Assess this cell for malaria.
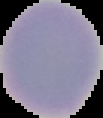
It is uninfected.

image_type: segmented cell region with the area outside set to black
preparation: thin blood smear
image_size: 103×118 pixels